Give the position of every Plasmodium parasite and every leukocyte.
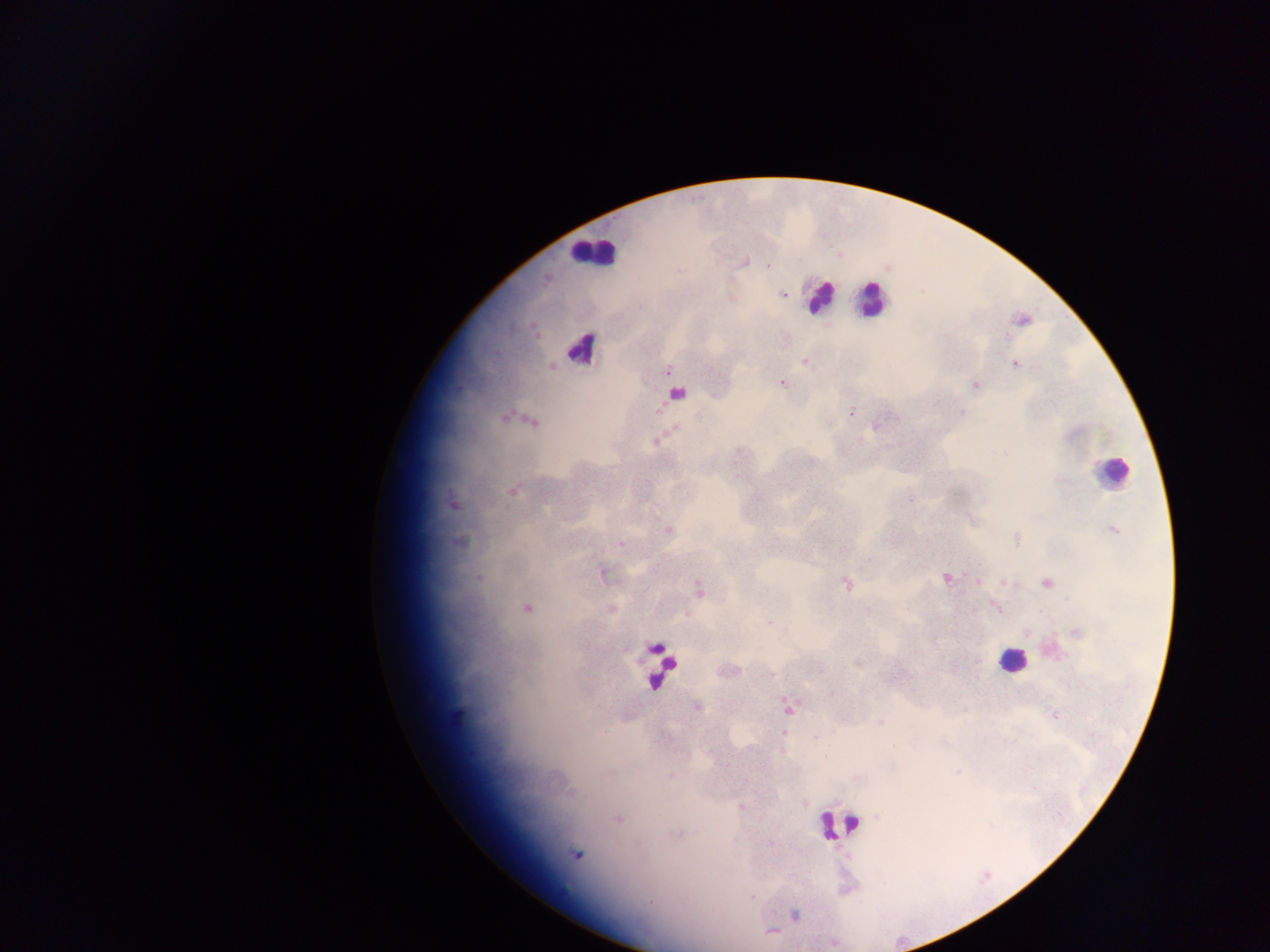
Approximate centers as [x, y] in pixels.
Plasmodium parasites: [768, 266], [783, 294], [805, 362], [1015, 364], [668, 372], [782, 383], [975, 385], [677, 393], [851, 412], [961, 412], [876, 426], [656, 441], [512, 490], [911, 500], [1114, 530], [668, 531], [620, 544], [602, 574], [478, 578], [946, 579], [978, 581], [1009, 582], [1047, 583], [846, 584], [698, 590], [996, 607], [527, 608], [611, 609], [769, 623], [977, 660], [832, 694], [696, 707], [789, 707], [458, 714], [1055, 715], [880, 722], [784, 732], [816, 737], [670, 776], [742, 807], [618, 818], [576, 854], [752, 897], [795, 914], [772, 932].
Leukocytes: [591, 252], [819, 297], [872, 300], [586, 351], [1111, 472], [1011, 661], [655, 662], [835, 825].

Summary:
  - Image size: 1270×952 pixels
  - Field of view: single
  - Country: Ghana
  - Preparation: thick blood film
  - Capture: mobile-phone photograph through a microscope